Identify the preparation type.
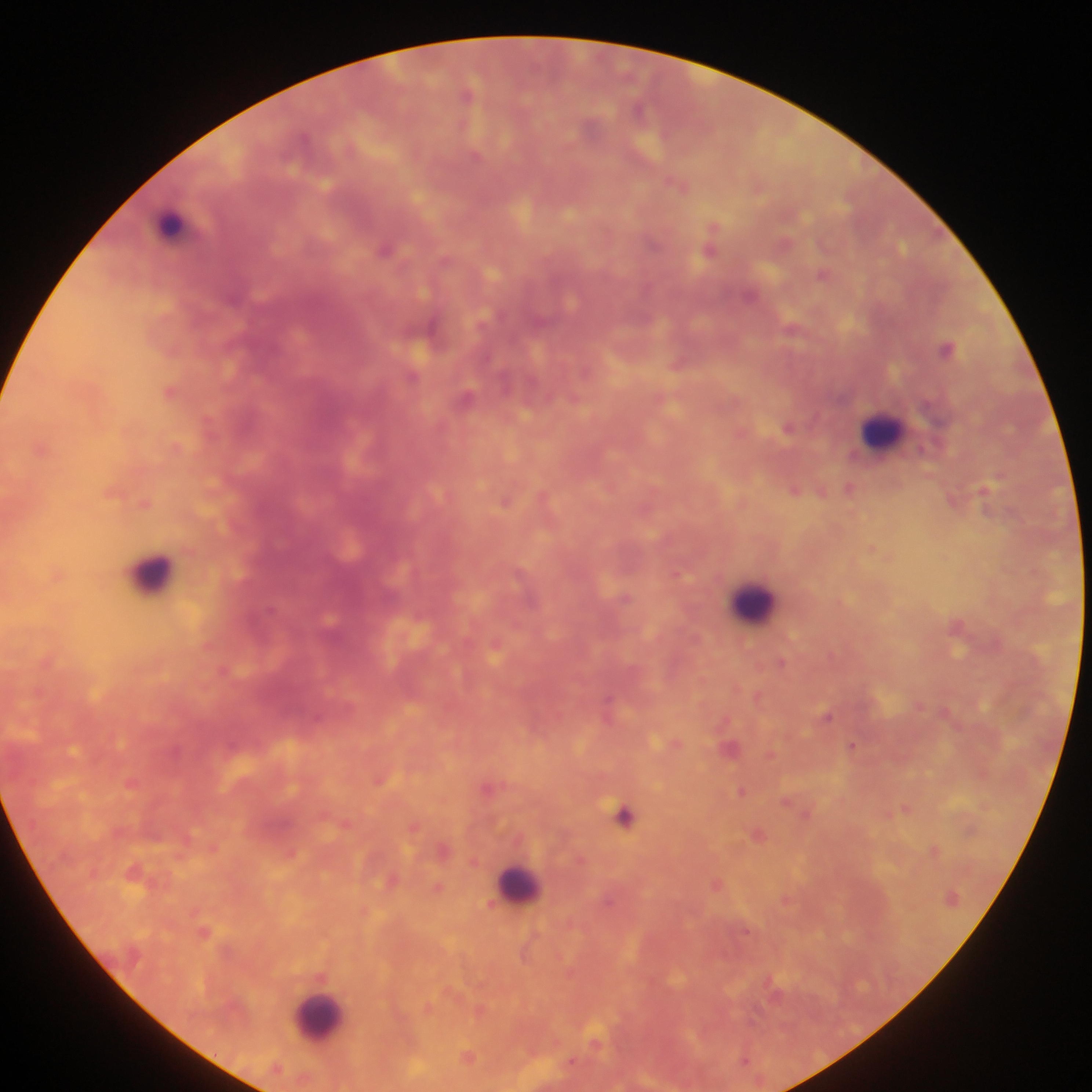

Thick blood film.

malaria parasite locations = approximate centers as x y in pixels: 468 93; 638 108; 679 184; 712 237; 786 242; 386 248; 710 250; 823 273; 793 328; 947 348; 679 363; 414 376; 170 391; 468 396; 575 397; 788 426; 175 446; 42 447; 850 487; 795 489; 823 492; 986 493; 544 496; 506 500; 146 503; 872 548; 57 574; 678 574; 625 597; 958 627; 495 646; 782 663; 224 670; 758 696; 608 705; 919 705; 828 716; 675 743; 853 745; 731 746; 770 753; 380 779; 132 782; 489 788; 742 791; 787 801; 905 807; 807 813; 625 815; 345 823; 414 826; 758 833; 213 847; 934 848; 445 849; 291 852; 580 859; 134 871; 392 881; 717 884; 439 887; 786 900; 746 930; 204 931; 481 1010; 597 1044; 468 1057; 746 1058; 572 1062
capture = mobile-phone photograph through a microscope
field of view = single
leukocyte locations = approximate centers as x y in pixels: 170 221; 881 431; 152 574; 753 603; 517 884; 319 1018
image size = 1092×1092 pixels
country = Ghana